State the blood parasite species.
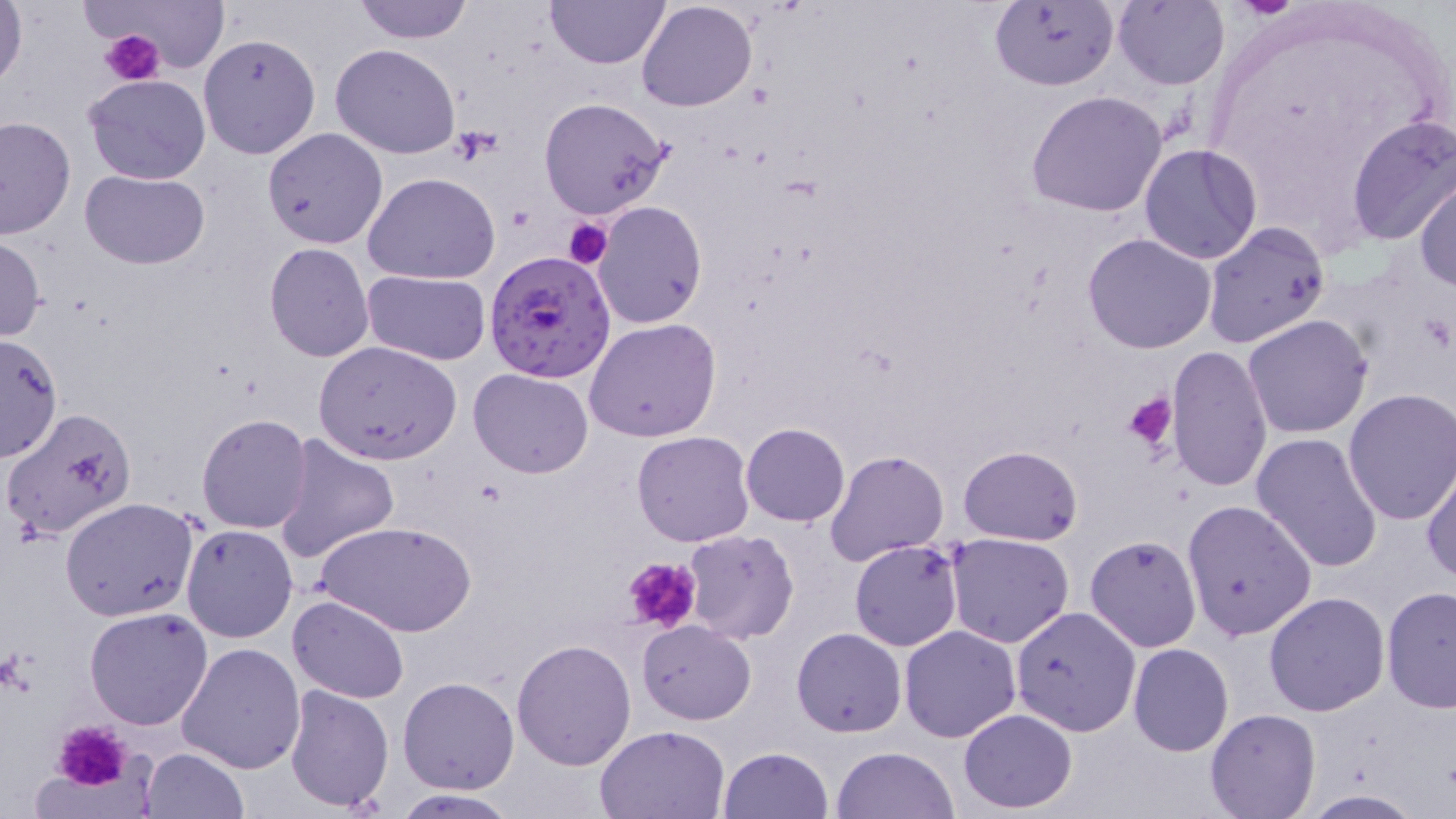

Plasmodium falciparum.

image size = 1456×819 pixels
platelet locations = approximate bounding boxes as (x1,y1)-(x2,y2) corner pairs in pixels: (100,29)-(164,86), (452,126)-(502,164), (563,217)-(613,269), (1123,389)-(1177,455), (620,556)-(702,635), (51,720)-(137,794)
stain = May-Grünwald-Giemsa
field of view = one of a larger specimen
Plasmodium falciparum-infected red blood cell locations = approximate bounding boxes as (x1,y1)-(x2,y2) corner pairs in pixels: (485,249)-(618,382)
preparation = thin blood film
modality = optical microscopy
magnification = 1000x
uninfected red blood cell locations = approximate bounding boxes as (x1,y1)-(x2,y2) corner pairs in pixels: (0,0)-(28,92), (351,0)-(475,44), (546,0)-(670,70), (988,0)-(1119,92), (1112,0)-(1229,89), (98,1)-(228,70), (637,1)-(758,113), (198,33)-(322,159), (330,43)-(460,159), (83,74)-(211,186), (1026,90)-(1168,218), (538,97)-(675,220), (1345,115)-(1456,248), (0,116)-(76,239), (262,127)-(388,249), (1138,144)-(1263,266), (79,170)-(209,269), (1412,171)-(1456,293), (363,172)-(500,284), (591,201)-(707,329), (1202,223)-(1331,350), (1084,231)-(1217,353), (0,236)-(47,342), (264,243)-(374,364), (361,269)-(490,364), (1242,314)-(1374,440), (584,318)-(722,443), (0,336)-(64,462), (313,340)-(462,464), (1165,346)-(1274,491), (469,367)-(595,478), (1341,388)-(1456,525), (3,406)-(136,540), (195,414)-(313,534), (742,422)-(849,527), (631,430)-(756,547), (272,433)-(400,564), (1252,434)-(1383,577), (958,445)-(1084,545), (824,450)-(948,568), (1421,460)-(1456,586), (643,474)-(760,612), (60,497)-(200,621), (1182,499)-(1318,640), (316,519)-(475,637), (181,524)-(298,643), (682,529)-(800,643), (946,532)-(1074,648), (1085,535)-(1201,652), (850,539)-(964,651), (1380,587)-(1456,712), (1263,592)-(1390,717), (288,594)-(409,704), (1010,605)-(1142,737), (84,606)-(215,731), (637,620)-(756,725), (898,626)-(1021,742), (792,627)-(906,737), (176,639)-(307,775), (512,639)-(636,770), (1127,643)-(1234,756), (398,676)-(518,794), (285,684)-(393,811), (958,708)-(1078,812), (1206,708)-(1320,819), (595,724)-(732,818), (719,746)-(833,819), (832,746)-(959,819), (139,747)-(249,818), (1299,789)-(1428,818), (389,790)-(521,818)